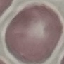
malaria_status: uninfected
preparation: thin blood film
image_type: automatically extracted cell patch, resized to 64 × 64 pixels
stain: Giemsa
capture: smartphone camera at the microscope eyepiece